State which parasite is depicted.
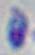
Toxoplasma gondii.

Summary:
  - Magnification: 1000x
  - Modality: photomicrograph